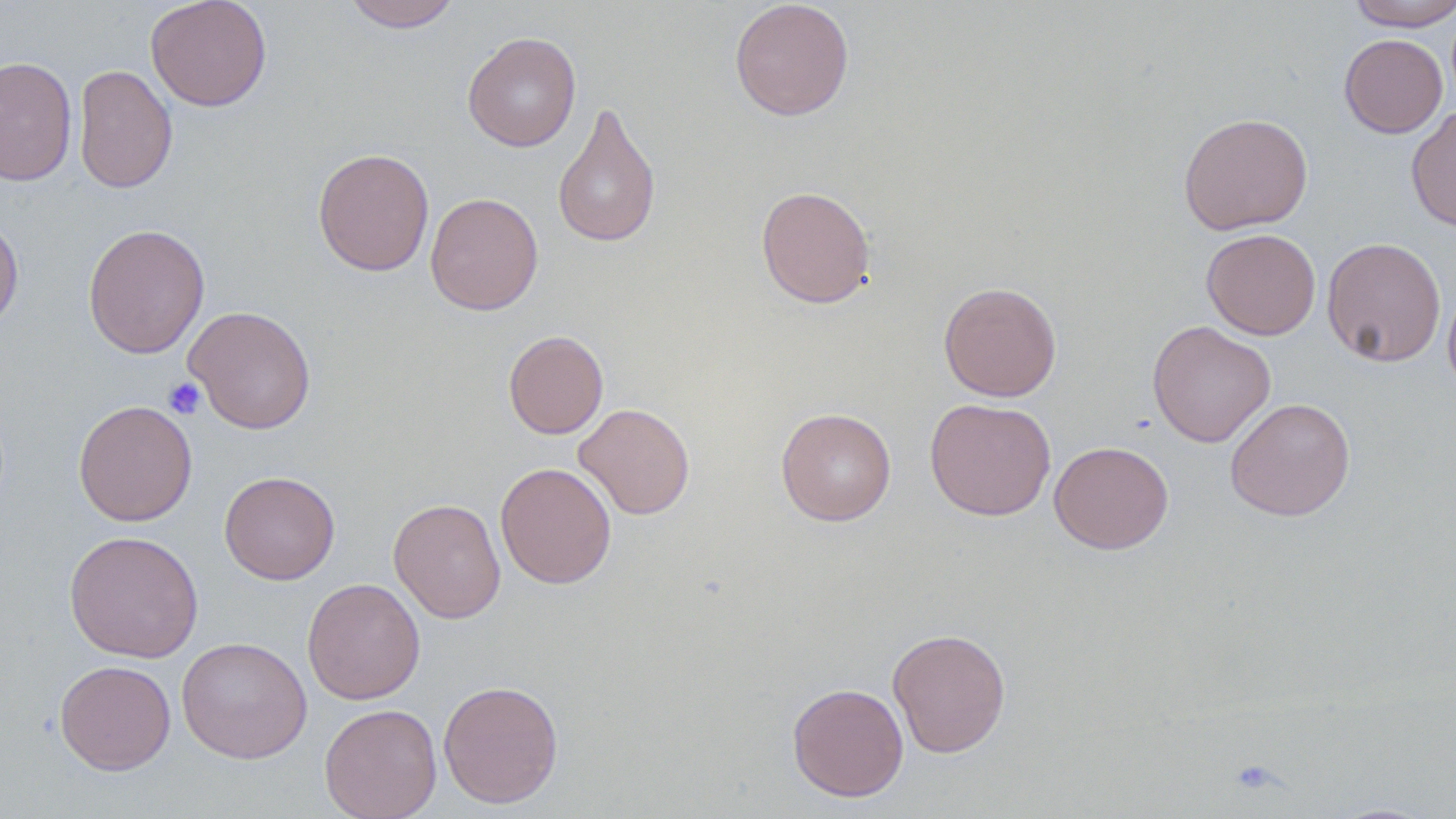 Approximate bounding boxes as named x1/y1/x2/y2 corners in pixels. Platelet locations: (x1=163, y1=377, x2=206, y2=419). Uninfected red blood cell locations: (x1=145, y1=0, x2=273, y2=112), (x1=340, y1=0, x2=461, y2=32), (x1=729, y1=0, x2=855, y2=121), (x1=1345, y1=0, x2=1456, y2=31), (x1=462, y1=31, x2=581, y2=152), (x1=1339, y1=34, x2=1448, y2=138), (x1=0, y1=56, x2=78, y2=187), (x1=73, y1=64, x2=177, y2=194), (x1=552, y1=100, x2=661, y2=249), (x1=1406, y1=105, x2=1456, y2=233), (x1=1178, y1=112, x2=1313, y2=235), (x1=312, y1=148, x2=434, y2=276), (x1=755, y1=185, x2=876, y2=309), (x1=425, y1=192, x2=543, y2=315), (x1=0, y1=213, x2=24, y2=334), (x1=82, y1=223, x2=210, y2=359), (x1=1201, y1=228, x2=1321, y2=340), (x1=1322, y1=237, x2=1447, y2=367), (x1=1443, y1=278, x2=1456, y2=398), (x1=938, y1=281, x2=1061, y2=401), (x1=183, y1=305, x2=317, y2=434), (x1=1147, y1=320, x2=1275, y2=448), (x1=503, y1=329, x2=609, y2=439), (x1=924, y1=397, x2=1056, y2=521), (x1=1225, y1=397, x2=1356, y2=522), (x1=73, y1=399, x2=198, y2=527), (x1=573, y1=402, x2=695, y2=520), (x1=775, y1=407, x2=896, y2=526), (x1=1049, y1=441, x2=1173, y2=554), (x1=495, y1=462, x2=617, y2=589), (x1=219, y1=470, x2=340, y2=585), (x1=388, y1=498, x2=506, y2=623), (x1=64, y1=530, x2=203, y2=662), (x1=302, y1=577, x2=426, y2=705), (x1=887, y1=627, x2=1012, y2=758), (x1=176, y1=636, x2=312, y2=764), (x1=55, y1=660, x2=176, y2=775), (x1=438, y1=679, x2=564, y2=809), (x1=787, y1=682, x2=909, y2=802), (x1=319, y1=703, x2=443, y2=819), (x1=1326, y1=802, x2=1442, y2=818). Slide-level diagnosis: no evidence of blood parasites. Single field of view. Captured at 1000x magnification. May-Grünwald-Giemsa stain. Image is 1456×819 pixels. Optical microscopy. Thin blood smear.